Report the malaria status of this cell.
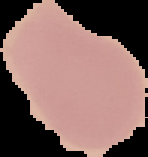
It is uninfected.

From a thin blood smear. Image is 148×157 pixels. The area outside the segmented cell region is set to black.